Locate every blood parasite and identify its species.
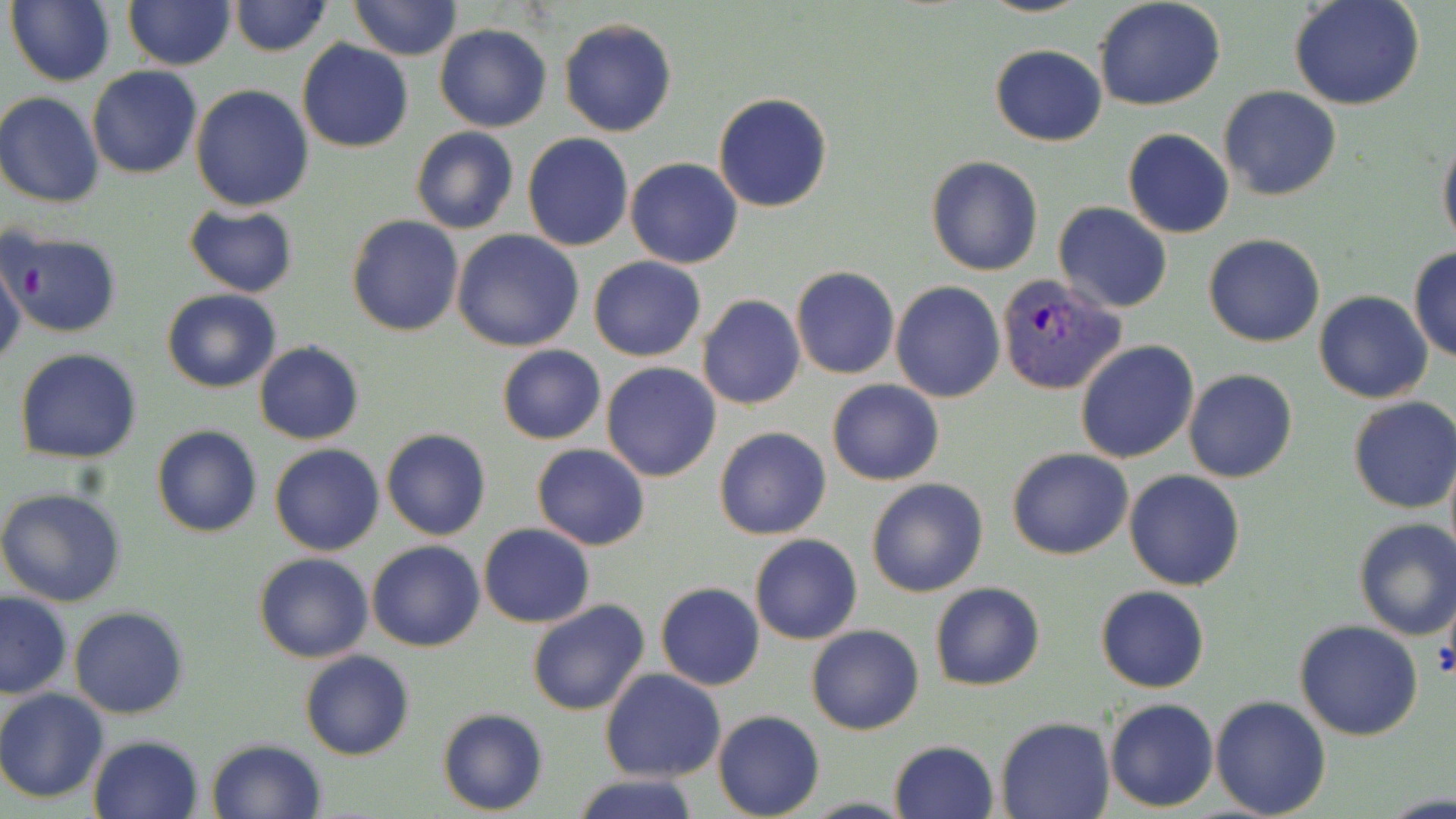

Approximate bounding boxes as (x1,y1)-(x2,y2) corner pairs in pixels.
Plasmodium vivax-infected red blood cells: (994,273)-(1125,396).
No Plasmodium falciparum, Plasmodium ovale, Plasmodium malariae, Babesia divergens, or Trypanosoma brucei observed.

Summary:
  - Uninfected red blood cell locations: (6,0)-(116,87), (347,0)-(463,60), (976,0)-(1091,18), (1093,0)-(1227,111), (122,1)-(236,70), (227,1)-(332,57), (1289,1)-(1424,111), (345,4)-(535,82), (558,18)-(677,137), (434,24)-(551,132), (297,39)-(414,153), (989,44)-(1108,146), (87,66)-(203,179), (189,83)-(312,212), (1219,85)-(1342,201), (713,92)-(834,213), (0,93)-(104,207), (410,127)-(517,234), (1438,128)-(1456,253), (1123,129)-(1234,239), (522,134)-(635,252), (928,155)-(1043,277), (626,158)-(743,269), (1052,202)-(1173,314), (183,204)-(299,297), (347,215)-(464,336), (1,230)-(122,339), (452,230)-(584,352), (1203,233)-(1326,348), (1408,248)-(1455,364), (589,256)-(706,361), (0,257)-(26,371), (790,267)-(900,379), (892,281)-(1005,402), (163,288)-(281,393), (1314,290)-(1431,403), (697,295)-(806,410), (1075,341)-(1198,464), (254,342)-(364,444), (496,345)-(606,445), (15,349)-(142,462), (602,363)-(721,482), (1184,369)-(1297,482), (827,380)-(943,485), (1347,396)-(1455,514), (151,424)-(261,538), (715,427)-(832,540), (381,428)-(490,541), (269,444)-(384,557), (532,444)-(649,550), (1007,448)-(1132,560), (1124,469)-(1247,590), (866,477)-(988,598), (0,489)-(127,608), (1352,518)-(1456,640), (479,523)-(596,628), (750,534)-(861,644), (367,540)-(485,653), (252,553)-(374,663), (654,582)-(765,690), (929,582)-(1045,691), (1094,585)-(1210,693), (0,592)-(73,699), (526,598)-(650,716), (68,606)-(188,720), (1295,620)-(1423,740), (807,624)-(925,735), (299,650)-(415,761), (600,669)-(726,782), (0,688)-(110,802), (1209,695)-(1330,818), (1104,698)-(1218,812), (437,709)-(549,815), (713,711)-(824,819), (996,717)-(1113,819), (87,733)-(205,819), (205,739)-(328,819), (888,740)-(998,819), (571,773)-(701,819)
  - Platelet locations: (19,262)-(47,299)
  - Slide-level diagnosis: Plasmodium vivax
  - Magnification: 1000x
  - Field of view: one of a larger specimen
  - Modality: optical microscopy
  - Image size: 1456×819 pixels
  - Stain: May-Grünwald-Giemsa
  - Preparation: thin blood film